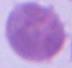

magnification = 1000x
modality = photomicrograph
identification = erythrocyte